Assess this cell for malaria.
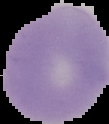
Uninfected.

Summary:
  - Preparation: thin blood film
  - Image size: 109×124 pixels
  - Image type: segmented cell region on a black background